Assess the morphology of the red blood cells.
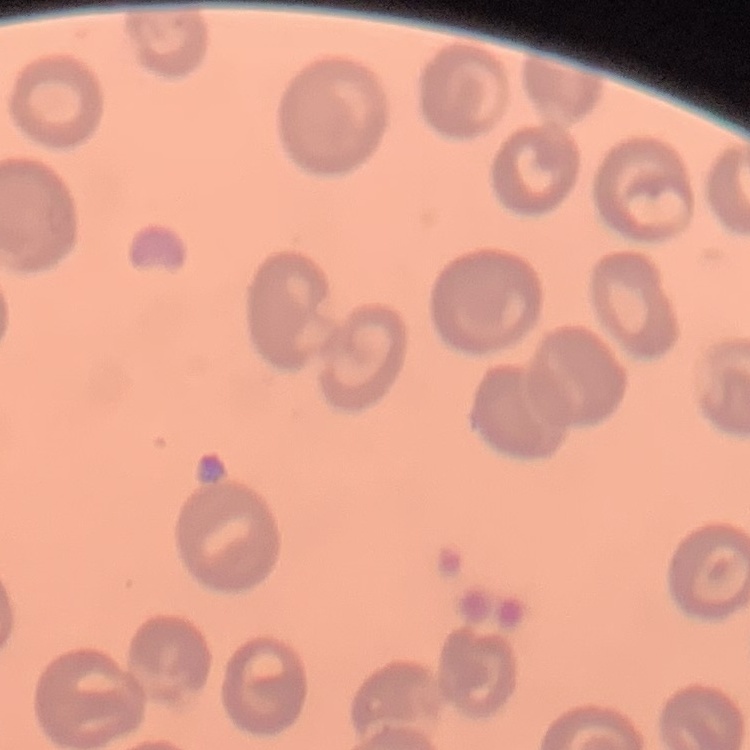

They show no rouleaux formation.

Summary:
  - Stain: Field's or Giemsa
  - Image type: one tile cut from a larger photomicrograph
  - Preparation: thin blood film